Locate every Plasmodium parasite.
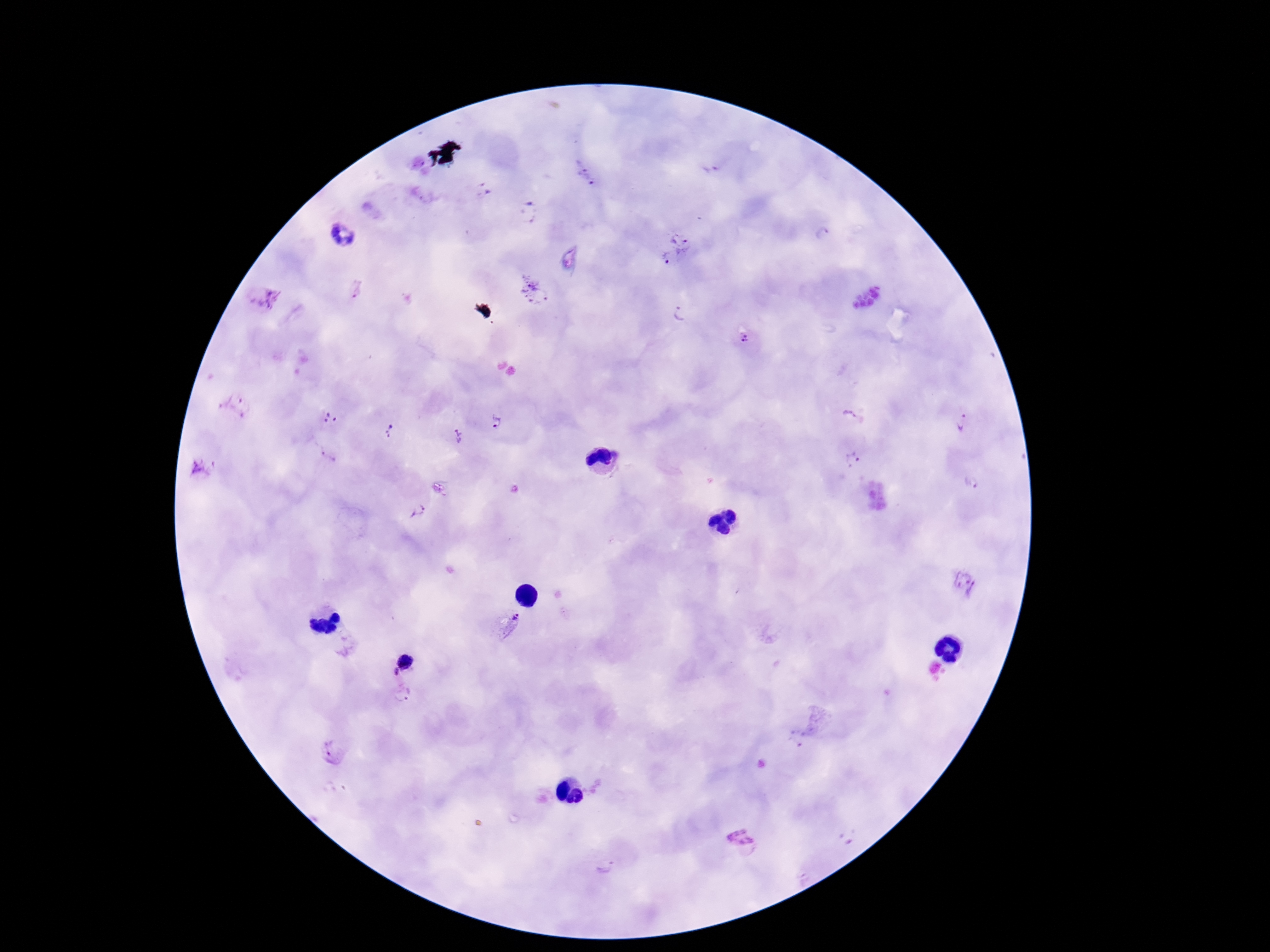

Approximate centers as (x, y) in pixels.
Plasmodium parasites: (586, 173), (483, 192), (529, 212), (343, 235), (681, 236), (823, 236), (667, 259), (356, 289), (532, 291), (262, 299), (679, 313), (744, 338), (235, 405), (850, 415), (330, 419), (962, 422), (496, 423), (390, 430), (458, 435), (326, 455), (851, 459), (205, 468), (971, 481), (415, 513), (964, 581), (510, 623), (406, 659), (392, 671), (403, 694), (793, 743), (332, 751), (743, 840), (609, 862).

capture: smartphone camera through the microscope eyepiece
image_size: 1270×952 pixels
field_of_view: single
stain: Giemsa
magnification: 100x
preparation: thick blood smear
patient_malaria_status: infected